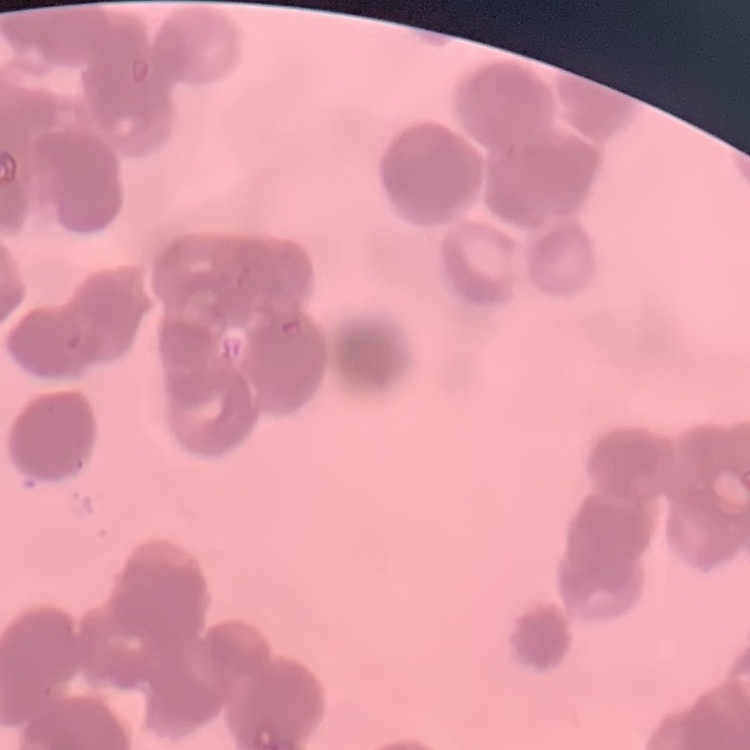
Summary:
  - Erythrocyte morphology: rouleaux formation
  - Preparation: thin blood film
  - Stain: Field's or Giemsa
  - Image type: square crop of a larger photomicrograph